Assess the morphology of the red blood cells.
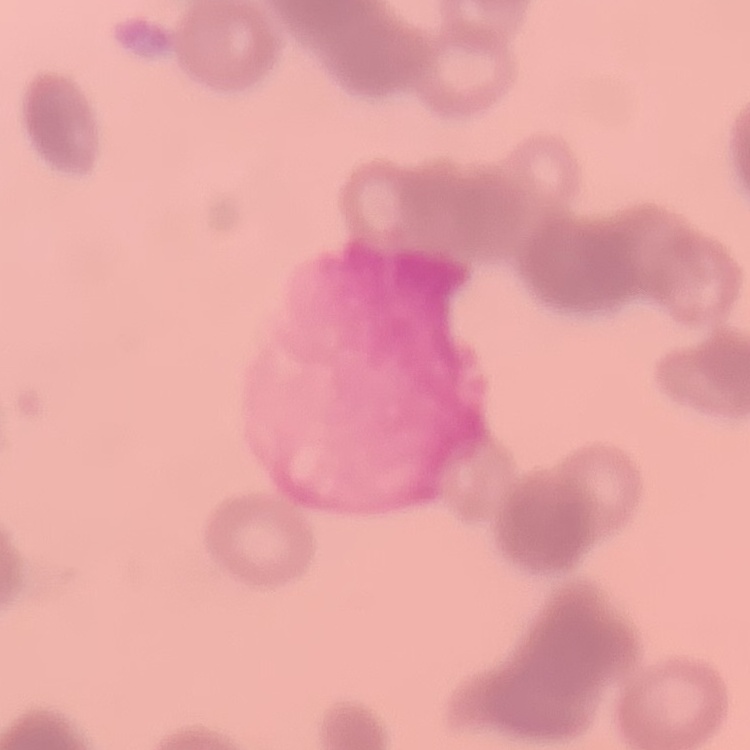
They show rouleaux formation.

Summary:
  - Stain: Field's or Giemsa
  - Preparation: thin blood smear
  - Image type: square crop of a larger photomicrograph